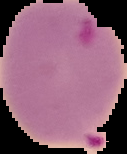
preparation: thin blood film
malaria_status: parasitized
image_size: 127×154 pixels
image_type: cell region segmented out of the field of view; surrounding area masked to black